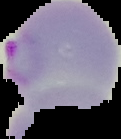
image type = cell region segmented out of the field of view; surrounding area masked to black
malaria status = parasitized
preparation = thin blood film
image size = 121×139 pixels